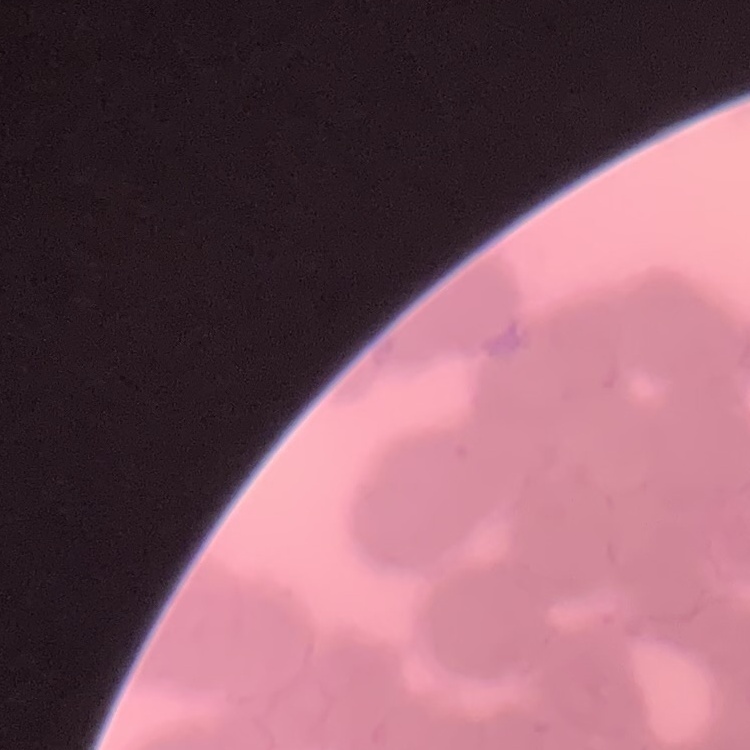

Summary:
  - Red blood cell morphology: rouleaux formation
  - Image type: square crop of a larger photomicrograph
  - Stain: Field's or Giemsa
  - Preparation: thin peripheral smear